Report the malaria status of this cell.
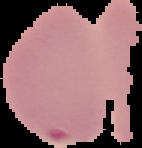
It is parasitized.

Image is 142×148 pixels. The area outside the segmented cell region is set to black. From a thin blood film.